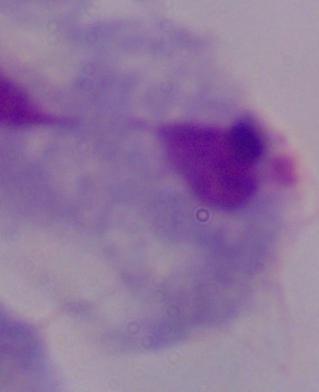 Photomicrograph. 1000x magnification. A trichomonad is shown.